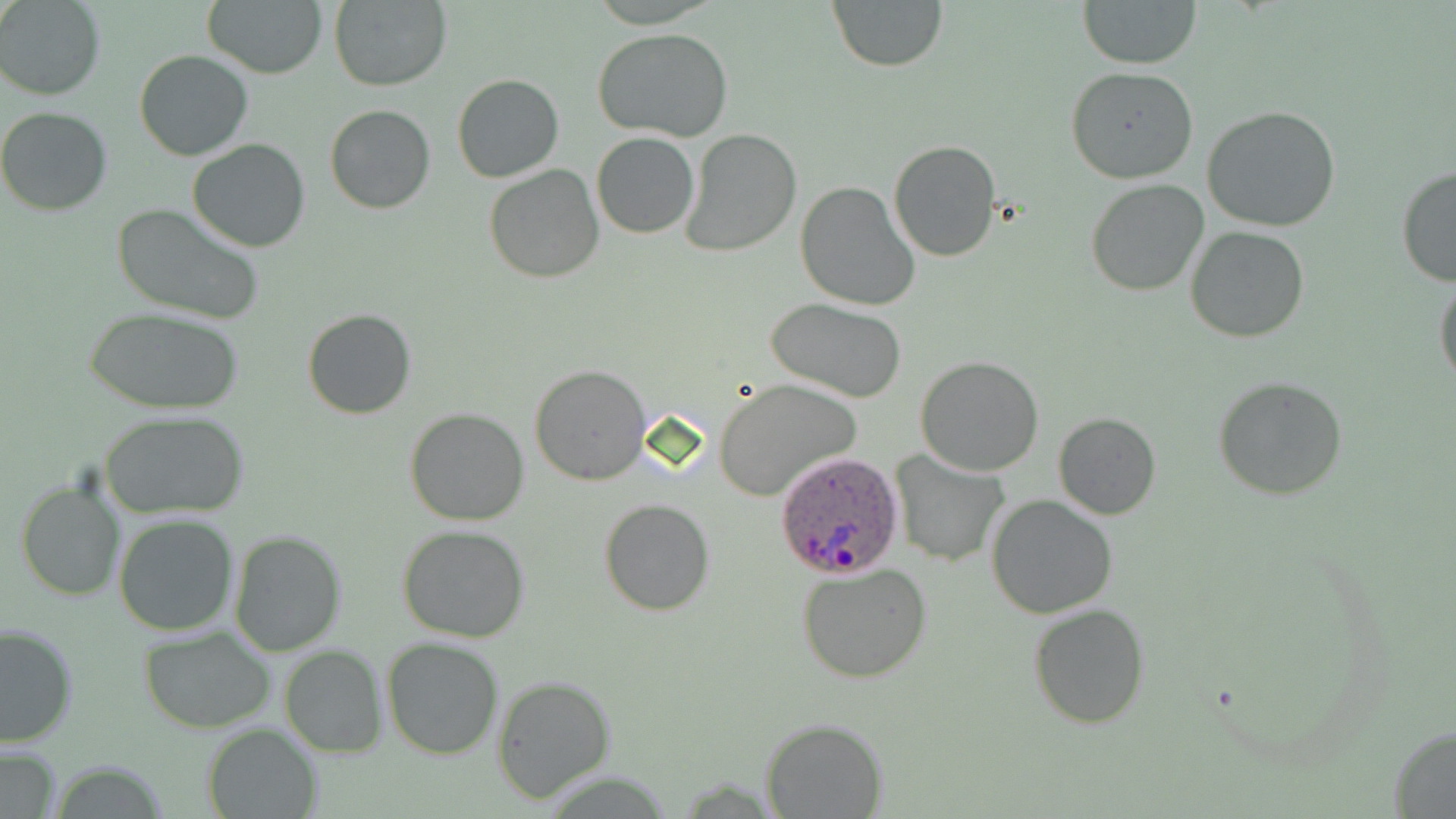

Approximate bounding boxes as [x1, y1, x2, y2] in pixels. Plasmodium ovale-infected red blood cell locations: [775, 449, 904, 579]. Uninfected red blood cell locations: [1, 0, 104, 100], [204, 0, 328, 78], [329, 0, 452, 91], [827, 0, 948, 72], [1077, 0, 1201, 69], [590, 28, 738, 143], [134, 50, 253, 160], [1066, 65, 1199, 185], [452, 73, 563, 184], [325, 104, 436, 214], [1201, 106, 1341, 233], [0, 107, 112, 215], [682, 128, 802, 257], [591, 132, 699, 239], [187, 139, 311, 253], [887, 139, 1001, 261], [483, 164, 603, 284], [1395, 164, 1456, 288], [1086, 180, 1210, 297], [795, 181, 922, 312], [110, 201, 266, 326], [1185, 227, 1311, 343], [1434, 274, 1456, 390], [764, 298, 912, 404], [302, 308, 416, 420], [85, 309, 241, 415], [915, 355, 1044, 477], [530, 364, 649, 484], [713, 378, 860, 499], [1214, 378, 1347, 499], [404, 408, 530, 526], [98, 410, 249, 520], [1052, 412, 1162, 519], [893, 451, 1010, 566], [15, 477, 127, 602], [985, 494, 1119, 619], [598, 498, 715, 615], [113, 516, 239, 636], [398, 523, 531, 642], [227, 529, 346, 656], [797, 562, 933, 682], [1026, 603, 1149, 730], [1, 623, 77, 749], [139, 627, 276, 731], [382, 636, 504, 759], [279, 645, 387, 757], [492, 676, 617, 804], [762, 717, 887, 818], [200, 722, 323, 819], [1387, 727, 1456, 817], [0, 743, 63, 819], [46, 762, 174, 818]. Slide-level diagnosis: Plasmodium ovale. One field of a larger specimen. Thin blood film. Image is 1456×819 pixels. 1000x magnification. Optical microscopy. May-Grünwald-Giemsa stain.